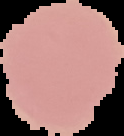

Summary:
  - Image type: segmented cell region on a black background
  - Preparation: thin blood film
  - Result: negative for Plasmodium parasites
  - Image size: 124×136 pixels